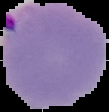

Summary:
  - Preparation: thin blood film
  - Malaria status: parasitized
  - Image size: 109×112 pixels
  - Image type: segmented cell region on a black background